Classify this cell by malaria status.
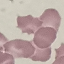
Uninfected.

Thin smear of blood. Automatically extracted cell patch, resized to 64 × 64 pixels. Photographed with a smartphone camera at the microscope eyepiece. Giemsa stain.